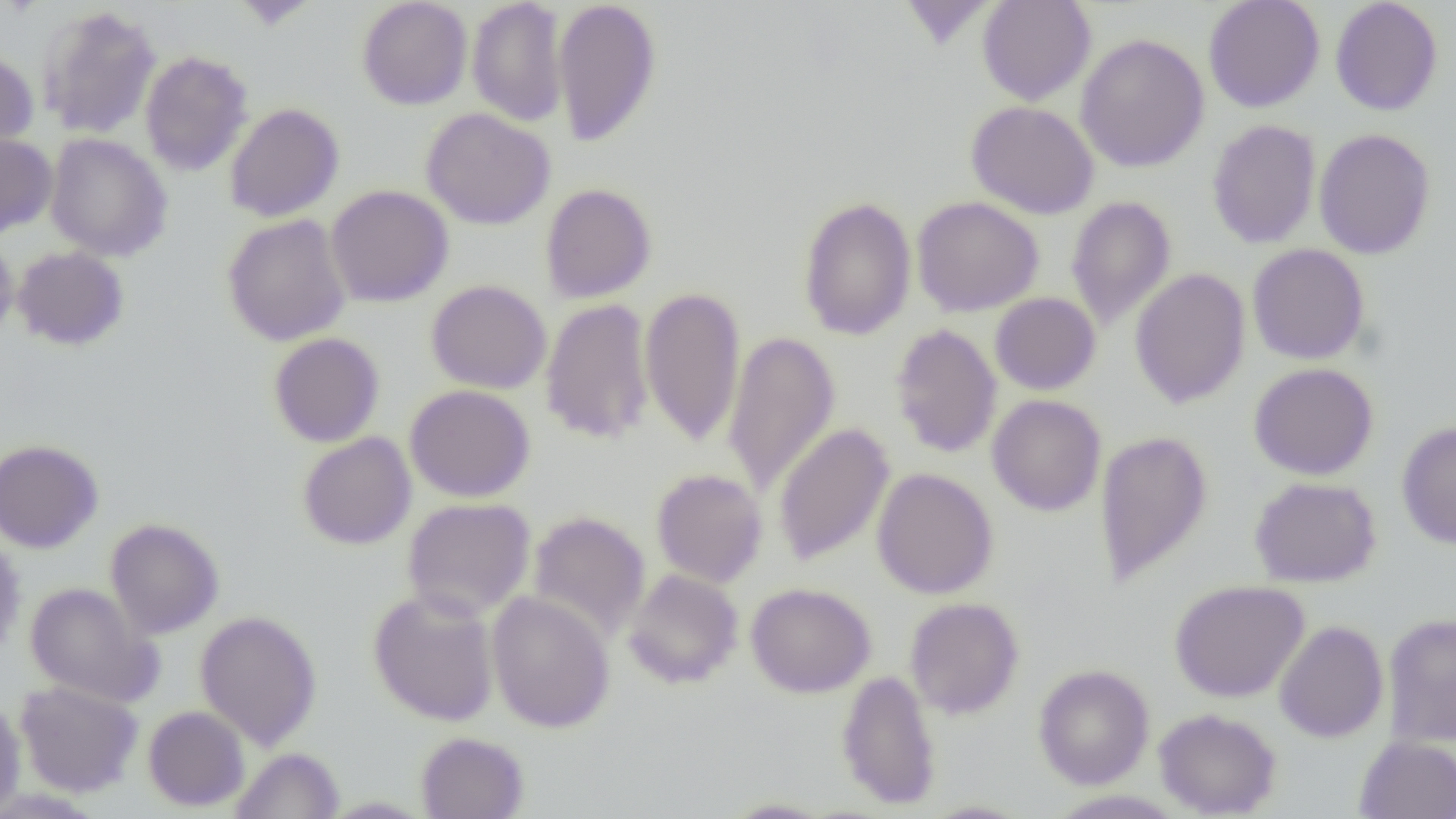
Summary:
  - Coordinate format: approximate bounding boxes as [x1, y1, x2, y2] in pixels
  - Uninfected red blood cell locations: [357, 0, 473, 110], [467, 0, 568, 127], [553, 0, 662, 147], [898, 0, 998, 51], [977, 0, 1095, 105], [1203, 0, 1325, 112], [1330, 0, 1443, 116], [233, 1, 316, 30], [38, 5, 162, 138], [1076, 33, 1210, 173], [0, 48, 39, 155], [140, 50, 254, 176], [966, 101, 1099, 219], [225, 102, 344, 222], [421, 108, 555, 230], [1207, 120, 1321, 248], [1313, 128, 1436, 259], [0, 133, 57, 238], [45, 133, 173, 262], [540, 183, 657, 303], [326, 185, 453, 308], [1065, 195, 1176, 329], [798, 196, 917, 341], [912, 196, 1044, 317], [222, 213, 352, 346], [0, 232, 19, 346], [1247, 243, 1370, 365], [12, 246, 129, 350], [1130, 268, 1250, 408], [426, 280, 552, 394], [639, 286, 746, 447], [990, 292, 1101, 395], [540, 297, 655, 445], [890, 323, 1003, 459], [722, 330, 840, 499], [269, 332, 384, 447], [1248, 362, 1379, 480], [405, 384, 535, 502], [987, 394, 1106, 516], [1396, 419, 1456, 549], [773, 422, 894, 566], [1094, 430, 1213, 586], [297, 431, 417, 550], [0, 438, 103, 553], [872, 467, 998, 599], [651, 468, 768, 587], [1249, 476, 1382, 588], [402, 497, 536, 620], [527, 511, 650, 642], [105, 518, 224, 639], [0, 536, 26, 660], [623, 569, 743, 689], [1169, 579, 1309, 703], [24, 582, 162, 707], [745, 582, 876, 698], [367, 587, 500, 727], [486, 591, 615, 733], [904, 597, 1024, 719], [195, 610, 322, 749], [1382, 612, 1456, 746], [1274, 620, 1388, 743], [1033, 664, 1154, 790], [836, 669, 942, 811], [14, 680, 144, 797], [0, 696, 27, 816], [143, 706, 250, 811], [1154, 708, 1282, 818], [415, 731, 529, 818], [1354, 736, 1456, 818], [231, 747, 344, 818], [1043, 790, 1188, 818], [319, 796, 435, 818], [721, 798, 834, 818], [917, 800, 1035, 819]
  - Slide-level diagnosis: negative for blood parasites
  - Preparation: thin blood smear
  - Image size: 1456×819 pixels
  - Field of view: single
  - Modality: light microscopy
  - Magnification: 1000x